Assess this cell for malaria.
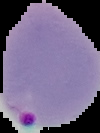

Parasitized.

Summary:
  - Image type: segmented cell region with the area outside set to black
  - Image size: 100×133 pixels
  - Preparation: thin blood smear